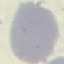
Summary:
  - Result: no malaria parasites seen
  - Preparation: thin blood film
  - Stain: Giemsa
  - Capture: smartphone through the microscope eyepiece
  - Image type: cell patch, automatically extracted from a larger field of view and resized to 64 × 64 pixels